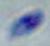
Summary:
  - Identification: Toxoplasma gondii
  - Magnification: 1000x
  - Modality: photomicrograph